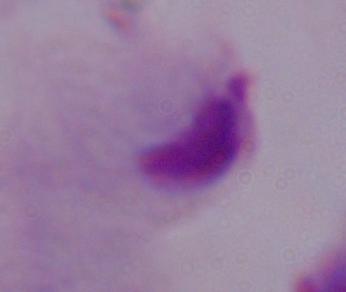 Photomicrograph. Captured at 1000x magnification. A trichomonad is shown.